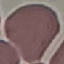
{
  "result": "no malaria parasites seen",
  "stain": "Giemsa",
  "capture": "smartphone through the microscope eyepiece",
  "image_type": "automatically extracted cell patch, resized to 64 × 64 pixels",
  "preparation": "thin blood smear"
}